Locate every blood parasite and identify its species.
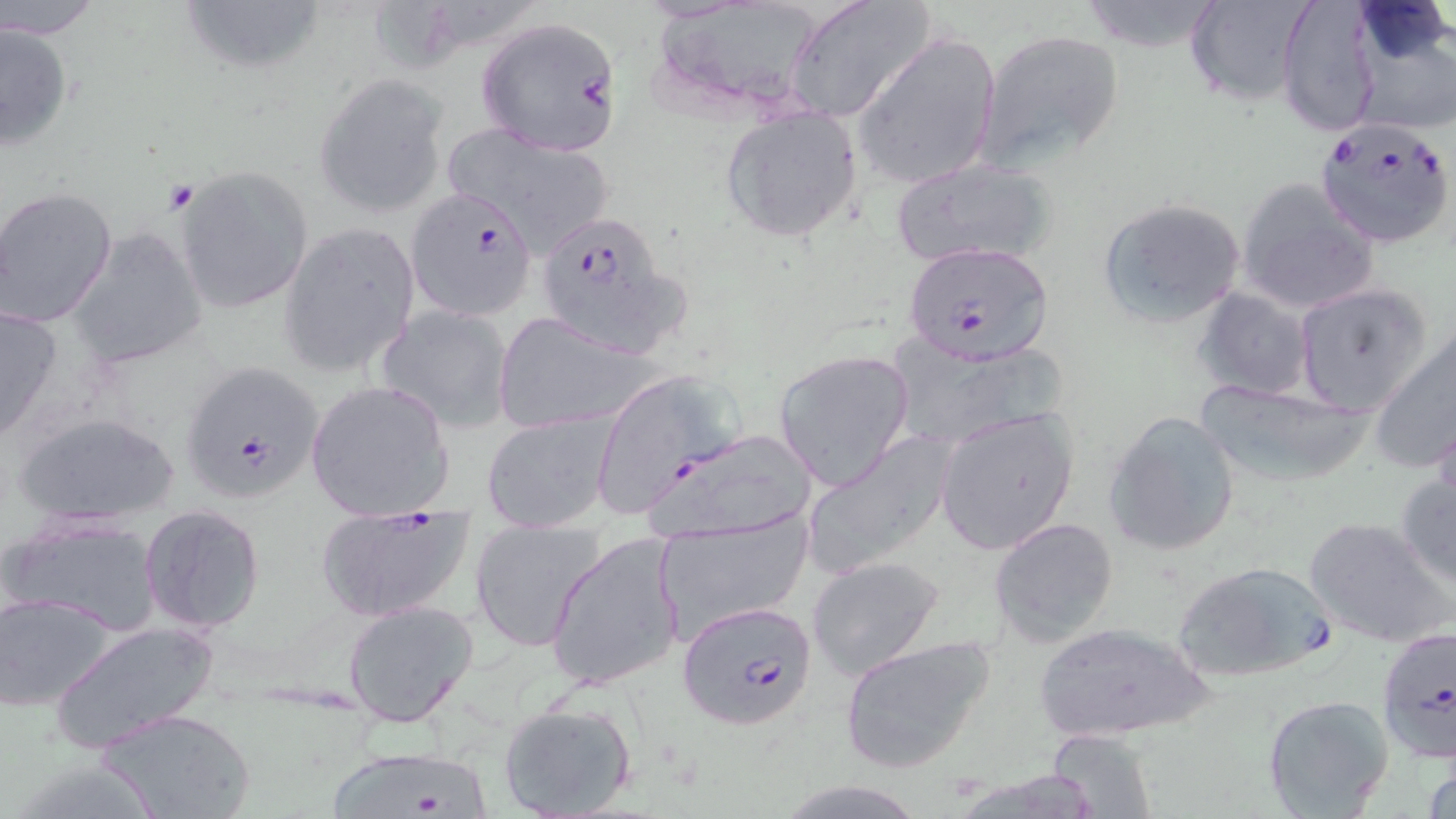

Approximate bounding boxes as named x1/y1/x2/y2 corners in pixels.
Plasmodium falciparum-infected red blood cells: (x1=474, y1=18, x2=625, y2=155), (x1=1315, y1=118, x2=1456, y2=249), (x1=404, y1=187, x2=543, y2=319), (x1=531, y1=208, x2=687, y2=360), (x1=904, y1=240, x2=1054, y2=364), (x1=180, y1=359, x2=327, y2=504), (x1=588, y1=371, x2=742, y2=520), (x1=314, y1=503, x2=478, y2=624), (x1=1171, y1=560, x2=1338, y2=683), (x1=677, y1=599, x2=819, y2=731), (x1=1376, y1=623, x2=1454, y2=763), (x1=319, y1=742, x2=497, y2=819).
No Plasmodium ovale, Plasmodium malariae, Plasmodium vivax, Babesia divergens, or Trypanosoma brucei observed.

Uninfected red blood cell locations: (x1=3, y1=0, x2=106, y2=38), (x1=784, y1=0, x2=936, y2=125), (x1=1078, y1=0, x2=1224, y2=53), (x1=1186, y1=0, x2=1316, y2=107), (x1=1275, y1=0, x2=1382, y2=137), (x1=174, y1=1, x2=330, y2=79), (x1=1347, y1=14, x2=1456, y2=136), (x1=0, y1=22, x2=74, y2=153), (x1=855, y1=28, x2=1001, y2=192), (x1=975, y1=28, x2=1125, y2=175), (x1=313, y1=72, x2=449, y2=219), (x1=719, y1=107, x2=864, y2=244), (x1=437, y1=124, x2=621, y2=256), (x1=887, y1=157, x2=1057, y2=269), (x1=176, y1=166, x2=312, y2=314), (x1=1237, y1=177, x2=1380, y2=316), (x1=1, y1=189, x2=119, y2=328), (x1=1096, y1=198, x2=1247, y2=328), (x1=279, y1=222, x2=421, y2=378), (x1=70, y1=226, x2=209, y2=369), (x1=1293, y1=284, x2=1432, y2=415), (x1=1194, y1=288, x2=1315, y2=402), (x1=0, y1=303, x2=63, y2=443), (x1=375, y1=304, x2=515, y2=432), (x1=491, y1=311, x2=660, y2=434), (x1=1367, y1=329, x2=1456, y2=474), (x1=773, y1=348, x2=916, y2=490), (x1=305, y1=379, x2=455, y2=521), (x1=1193, y1=381, x2=1375, y2=487), (x1=936, y1=408, x2=1082, y2=553), (x1=12, y1=410, x2=182, y2=529), (x1=482, y1=410, x2=617, y2=532), (x1=1102, y1=411, x2=1242, y2=558), (x1=643, y1=428, x2=820, y2=544), (x1=800, y1=429, x2=955, y2=582), (x1=1395, y1=470, x2=1456, y2=590), (x1=138, y1=504, x2=265, y2=634), (x1=655, y1=513, x2=813, y2=636), (x1=988, y1=516, x2=1119, y2=648), (x1=1304, y1=516, x2=1452, y2=647), (x1=4, y1=517, x2=166, y2=636), (x1=470, y1=518, x2=604, y2=651), (x1=545, y1=532, x2=687, y2=692), (x1=808, y1=554, x2=945, y2=680), (x1=0, y1=593, x2=116, y2=713), (x1=340, y1=599, x2=481, y2=728), (x1=49, y1=618, x2=222, y2=752), (x1=1029, y1=621, x2=1216, y2=743), (x1=837, y1=635, x2=995, y2=773), (x1=1262, y1=694, x2=1395, y2=817), (x1=497, y1=698, x2=638, y2=818), (x1=100, y1=707, x2=253, y2=819), (x1=1045, y1=728, x2=1159, y2=817), (x1=774, y1=779, x2=930, y2=818). Slide-level diagnosis: Plasmodium falciparum. May-Grünwald-Giemsa stain. Optical microscopy. Thin blood smear. Single field of view. Captured at 1000x magnification. Image is 1456×819 pixels.